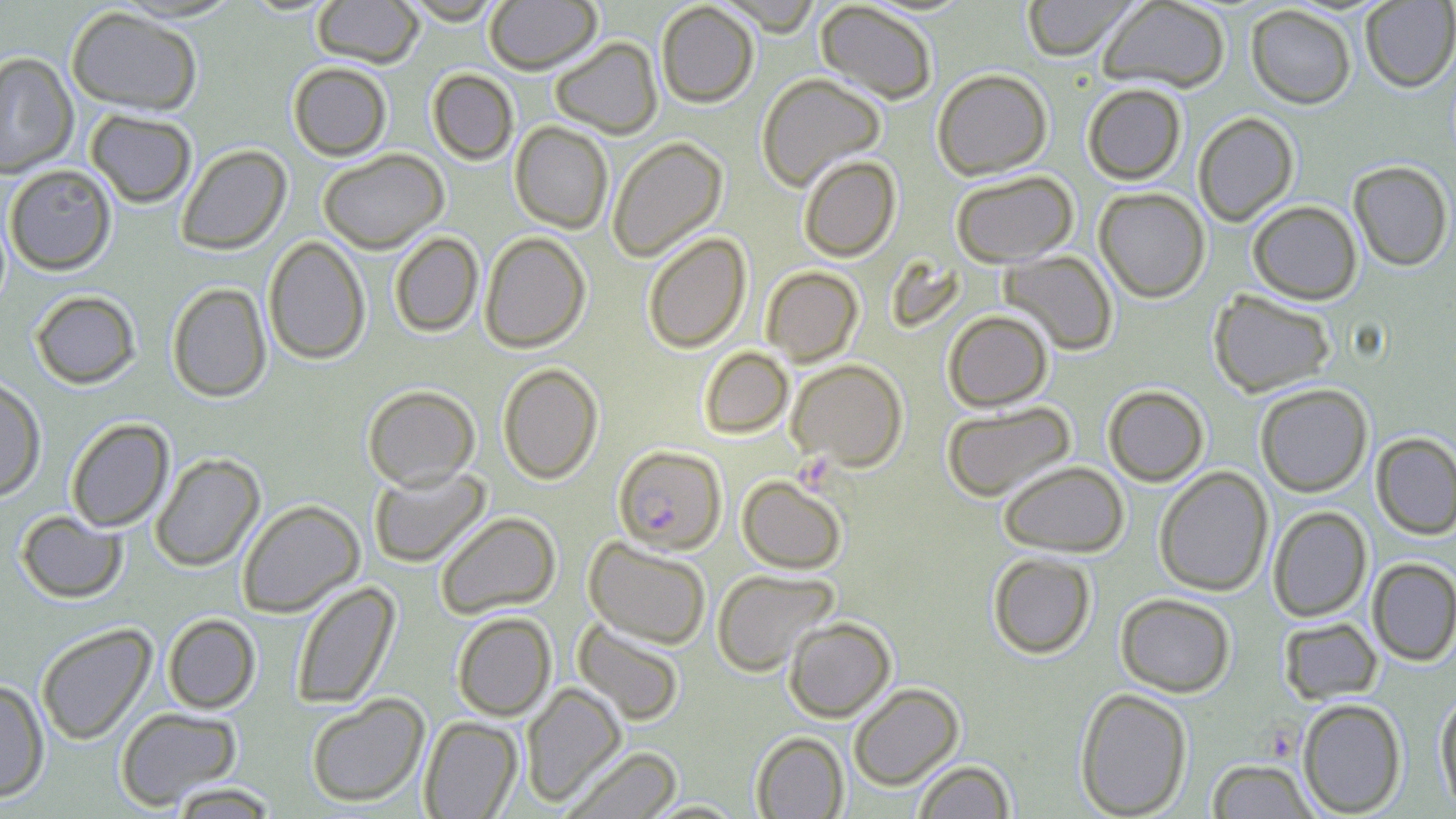
slide_level_diagnosis: Plasmodium falciparum
uninfected_red_blood_cell_locations: 'approximate bounding boxes as named x1/y1/x2/y2 corners in pixels: (x1=311, y1=0, x2=424, y2=68), (x1=399, y1=0, x2=508, y2=24), (x1=484, y1=0, x2=602, y2=74), (x1=716, y1=0, x2=822, y2=36), (x1=1021, y1=0, x2=1140, y2=60), (x1=1097, y1=0, x2=1231, y2=93), (x1=815, y1=1, x2=939, y2=105), (x1=1360, y1=1, x2=1456, y2=92), (x1=655, y1=2, x2=759, y2=107), (x1=1246, y1=4, x2=1357, y2=109), (x1=65, y1=6, x2=203, y2=116), (x1=550, y1=36, x2=662, y2=139), (x1=0, y1=52, x2=78, y2=178), (x1=288, y1=61, x2=393, y2=161), (x1=426, y1=68, x2=519, y2=165), (x1=932, y1=68, x2=1053, y2=180), (x1=756, y1=72, x2=886, y2=191), (x1=1082, y1=82, x2=1187, y2=184), (x1=85, y1=109, x2=197, y2=208), (x1=1192, y1=112, x2=1299, y2=226), (x1=510, y1=121, x2=614, y2=233), (x1=606, y1=136, x2=728, y2=262), (x1=176, y1=144, x2=291, y2=255), (x1=318, y1=148, x2=448, y2=254), (x1=798, y1=155, x2=900, y2=262), (x1=1348, y1=160, x2=1454, y2=271), (x1=4, y1=164, x2=117, y2=276), (x1=950, y1=169, x2=1079, y2=268), (x1=1094, y1=187, x2=1210, y2=303), (x1=1247, y1=200, x2=1362, y2=304), (x1=479, y1=231, x2=591, y2=353), (x1=389, y1=232, x2=484, y2=337), (x1=642, y1=232, x2=751, y2=353), (x1=263, y1=236, x2=371, y2=365), (x1=999, y1=250, x2=1119, y2=356), (x1=761, y1=266, x2=863, y2=366), (x1=166, y1=282, x2=272, y2=402), (x1=1208, y1=289, x2=1336, y2=397), (x1=30, y1=290, x2=141, y2=389), (x1=943, y1=310, x2=1053, y2=411), (x1=699, y1=346, x2=793, y2=439), (x1=787, y1=359, x2=908, y2=471), (x1=497, y1=363, x2=603, y2=484), (x1=0, y1=376, x2=46, y2=501), (x1=1255, y1=383, x2=1373, y2=497), (x1=363, y1=384, x2=480, y2=490), (x1=1102, y1=385, x2=1210, y2=486), (x1=942, y1=401, x2=1076, y2=503), (x1=65, y1=418, x2=174, y2=532), (x1=1371, y1=433, x2=1456, y2=540), (x1=150, y1=453, x2=265, y2=571), (x1=998, y1=461, x2=1129, y2=557), (x1=368, y1=466, x2=490, y2=568), (x1=1154, y1=466, x2=1273, y2=597), (x1=737, y1=475, x2=848, y2=574), (x1=237, y1=499, x2=365, y2=617), (x1=1267, y1=505, x2=1372, y2=622), (x1=16, y1=510, x2=127, y2=603), (x1=435, y1=511, x2=561, y2=619), (x1=584, y1=537, x2=712, y2=649), (x1=987, y1=551, x2=1096, y2=659), (x1=1367, y1=558, x2=1456, y2=666), (x1=711, y1=568, x2=838, y2=676), (x1=290, y1=580, x2=400, y2=710), (x1=1115, y1=592, x2=1236, y2=697), (x1=452, y1=612, x2=557, y2=720), (x1=162, y1=613, x2=261, y2=714), (x1=783, y1=616, x2=896, y2=722), (x1=1278, y1=617, x2=1383, y2=704), (x1=573, y1=619, x2=686, y2=726), (x1=36, y1=623, x2=157, y2=745), (x1=0, y1=679, x2=50, y2=802), (x1=521, y1=682, x2=626, y2=806), (x1=848, y1=682, x2=964, y2=790), (x1=1074, y1=687, x2=1194, y2=818), (x1=1435, y1=692, x2=1456, y2=813), (x1=305, y1=694, x2=429, y2=808), (x1=1297, y1=698, x2=1407, y2=816), (x1=114, y1=706, x2=243, y2=810), (x1=419, y1=716, x2=523, y2=818), (x1=751, y1=731, x2=849, y2=819), (x1=563, y1=746, x2=682, y2=819), (x1=1206, y1=759, x2=1319, y2=818), (x1=911, y1=760, x2=1017, y2=818), (x1=166, y1=782, x2=281, y2=818), (x1=640, y1=800, x2=749, y2=818)'
preparation: thin blood smear
field_of_view: single
magnification: 1000x
plasmodium_falciparum_infected_red_blood_cell_locations: 'approximate bounding boxes as named x1/y1/x2/y2 corners in pixels: (x1=613, y1=445, x2=727, y2=554)'
image_size: 1456×819 pixels
stain: May-Grünwald-Giemsa
modality: light microscopy
platelet_locations: 'approximate bounding boxes as named x1/y1/x2/y2 corners in pixels: (x1=794, y1=454, x2=837, y2=493), (x1=1256, y1=719, x2=1308, y2=765)'